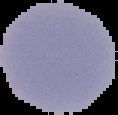
Summary:
  - Result: no Plasmodium parasites seen
  - Image size: 118×115 pixels
  - Image type: cell region segmented out of the field of view; surrounding area masked to black
  - Preparation: thin blood film